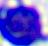
magnification = 400x
identification = leukocyte
modality = photomicrograph